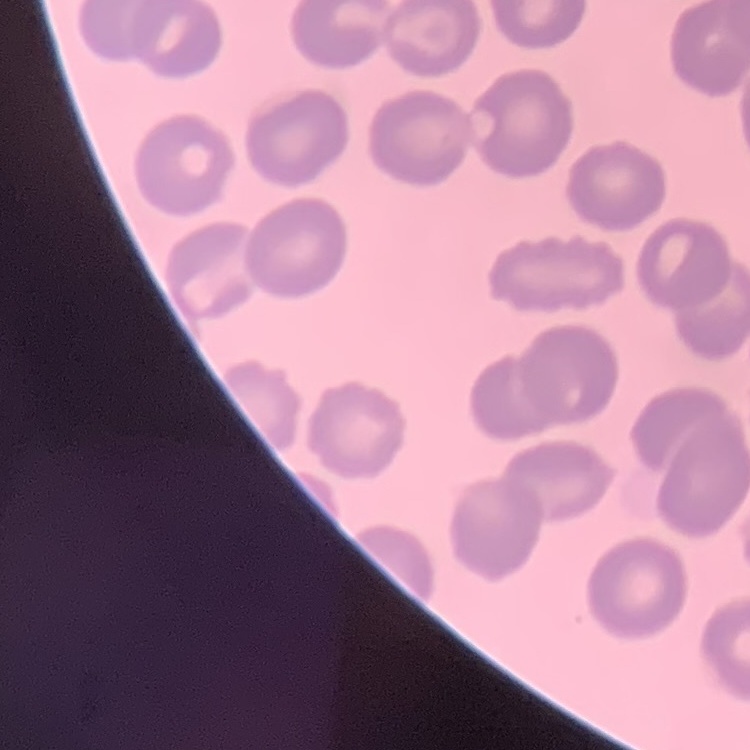

Summary:
  - Erythrocyte morphology: no rouleaux formation
  - Preparation: thin blood smear
  - Image type: square crop of a larger photomicrograph
  - Stain: Field's or Giemsa